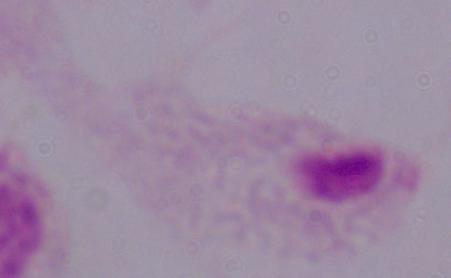 Captured at 1000x magnification. A trichomonad is shown. Photomicrograph.